Outline each blood parasite and name the species.
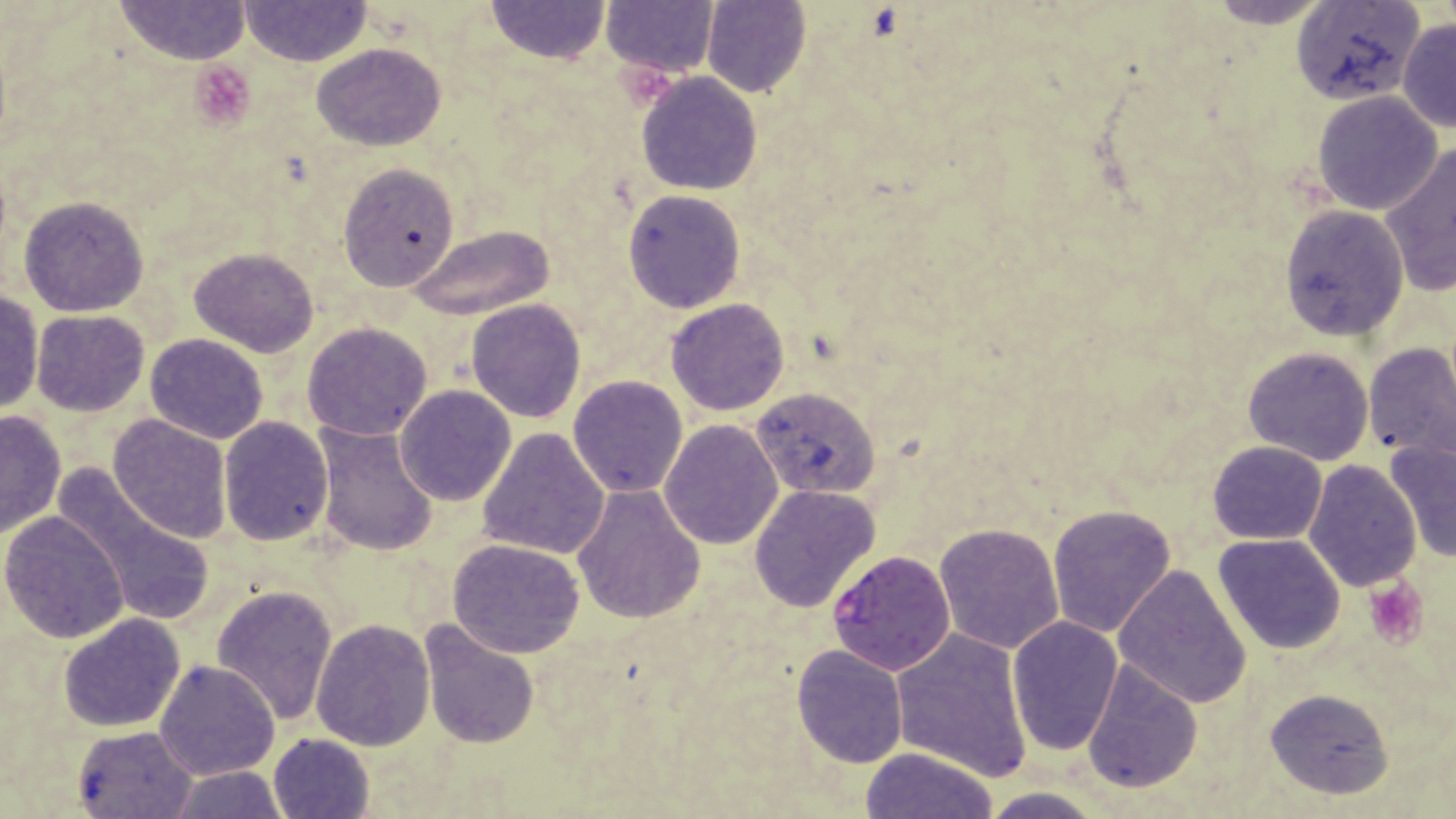

Approximate bounding boxes as (x1,y1)-(x2,y2) corner pairs in pixels.
Plasmodium falciparum-infected red blood cells: (827,550)-(957,675).
No Plasmodium ovale, Plasmodium malariae, Plasmodium vivax, Babesia divergens, or Trypanosoma brucei observed.

slide_level_diagnosis: Plasmodium falciparum
stain: May-Grünwald-Giemsa
modality: optical microscopy
image_size: 1456×819 pixels
preparation: thin blood smear
platelet_locations: 'approximate bounding boxes as (x1,y1)-(x2,y2) corner pairs in pixels: (191,63)-(255,126), (1365,577)-(1426,649)'
field_of_view: one of a larger specimen
magnification: 1000x
uninfected_red_blood_cell_locations: 'approximate bounding boxes as (x1,y1)-(x2,y2) corner pairs in pixels: (1196,0)-(1343,26), (116,1)-(248,65), (487,1)-(609,63), (1289,1)-(1425,106), (241,2)-(369,65), (601,2)-(720,79), (702,2)-(811,97), (1397,19)-(1455,133), (312,42)-(445,151), (636,73)-(763,194), (1312,90)-(1443,215), (1378,141)-(1455,297), (336,163)-(460,293), (622,190)-(745,313), (18,196)-(149,317), (1278,204)-(1409,341), (408,224)-(556,322), (188,248)-(320,357), (1,286)-(44,417), (466,298)-(585,423), (664,298)-(790,416), (31,310)-(151,417), (302,322)-(433,441), (145,333)-(268,443), (1363,343)-(1456,460), (1242,345)-(1375,465), (567,374)-(688,498), (395,385)-(516,506), (751,386)-(881,499), (0,408)-(66,538), (108,413)-(232,542), (217,416)-(333,547), (659,419)-(784,550), (311,423)-(439,557), (477,427)-(609,560), (1384,438)-(1456,564), (1208,441)-(1327,545), (1302,458)-(1421,592), (54,463)-(216,631), (571,484)-(706,624), (748,484)-(879,613), (1047,503)-(1176,639), (0,512)-(129,644), (934,521)-(1066,653), (1213,533)-(1346,656), (446,537)-(587,658), (1112,564)-(1252,708), (212,585)-(341,726), (58,612)-(185,731), (1006,617)-(1124,757), (311,619)-(435,751), (422,622)-(539,748), (891,629)-(1032,781), (791,645)-(908,767), (1081,659)-(1202,794), (154,661)-(280,781), (1264,688)-(1393,800), (72,725)-(196,818), (267,733)-(377,819), (862,747)-(999,819), (165,765)-(289,819), (975,786)-(1107,819)'